Comment on the morphology of the erythrocytes.
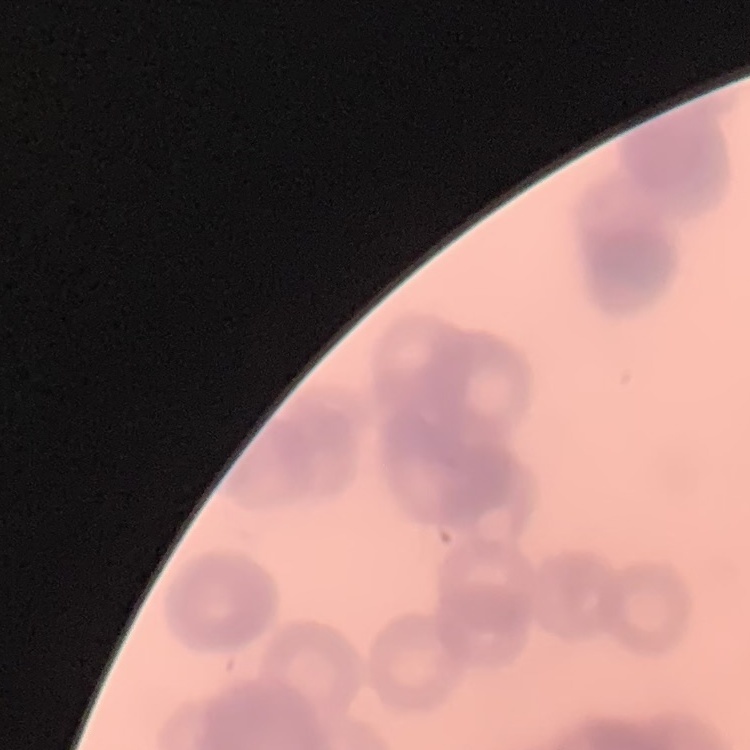
Rouleaux formation.

Field's or Giemsa stain. Square crop of a larger photomicrograph. Thin blood smear.